Locate every blood parasite and identify its species.
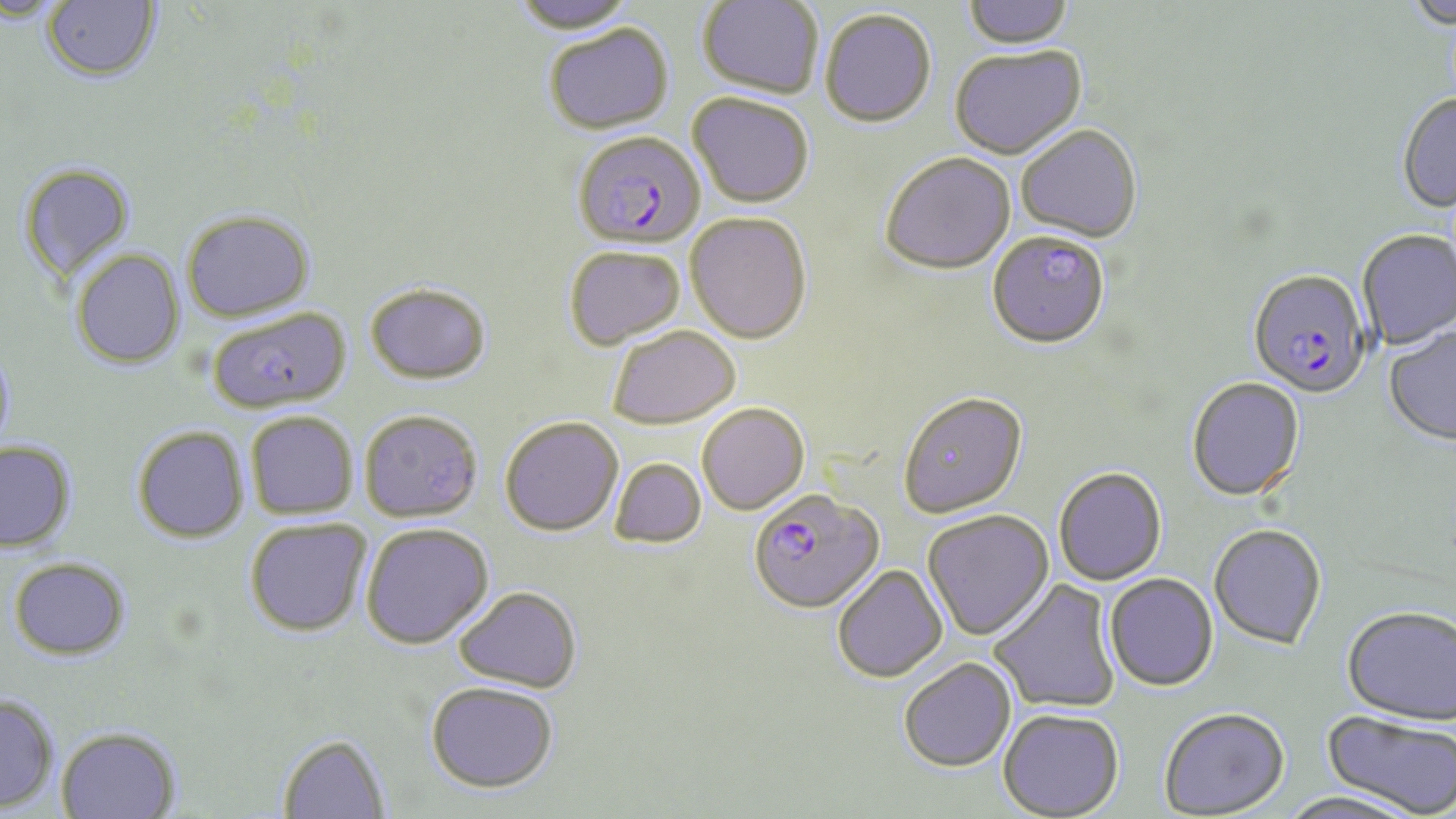

Approximate bounding boxes as (x1,y1)-(x2,y2) corner pairs in pixels.
Plasmodium falciparum-infected red blood cells: (573,131)-(705,250), (1247,271)-(1370,399), (749,489)-(883,613).
No Plasmodium ovale, Plasmodium malariae, Plasmodium vivax, Babesia divergens, or Trypanosoma brucei observed.

Uninfected red blood cell locations: (42,0)-(161,83), (510,0)-(640,35), (698,0)-(823,98), (962,0)-(1075,51), (0,1)-(69,26), (1403,1)-(1456,30), (819,9)-(936,128), (544,24)-(674,135), (950,47)-(1087,161), (687,92)-(814,208), (1397,94)-(1456,214), (1016,126)-(1143,244), (880,153)-(1015,276), (17,163)-(136,284), (181,210)-(315,323), (685,213)-(812,344), (1357,229)-(1456,351), (987,233)-(1110,350), (564,246)-(685,350), (71,248)-(185,369), (364,282)-(491,385), (207,308)-(352,414), (1383,325)-(1456,447), (607,326)-(741,430), (0,341)-(16,458), (1186,378)-(1305,502), (898,392)-(1028,518), (697,403)-(810,515), (360,410)-(483,523), (246,412)-(358,519), (500,417)-(623,537), (132,425)-(249,543), (0,440)-(76,552), (610,458)-(706,548), (1053,467)-(1167,585), (922,509)-(1054,641), (244,518)-(372,637), (361,523)-(493,649), (1209,525)-(1327,650), (9,557)-(131,660), (832,564)-(947,683), (1104,573)-(1219,692), (989,579)-(1121,715), (454,586)-(582,693), (1342,606)-(1456,727), (898,657)-(1016,772), (426,680)-(558,793), (0,693)-(59,812), (1159,707)-(1290,817), (998,708)-(1124,818), (1320,711)-(1456,817), (56,726)-(182,819), (278,733)-(390,819), (1279,790)-(1425,819). Slide-level diagnosis: Plasmodium falciparum. Image is 1456×819 pixels. Single field of view. Thin blood smear. 1000x magnification. May-Grünwald-Giemsa-stained preparation. Optical microscopy.